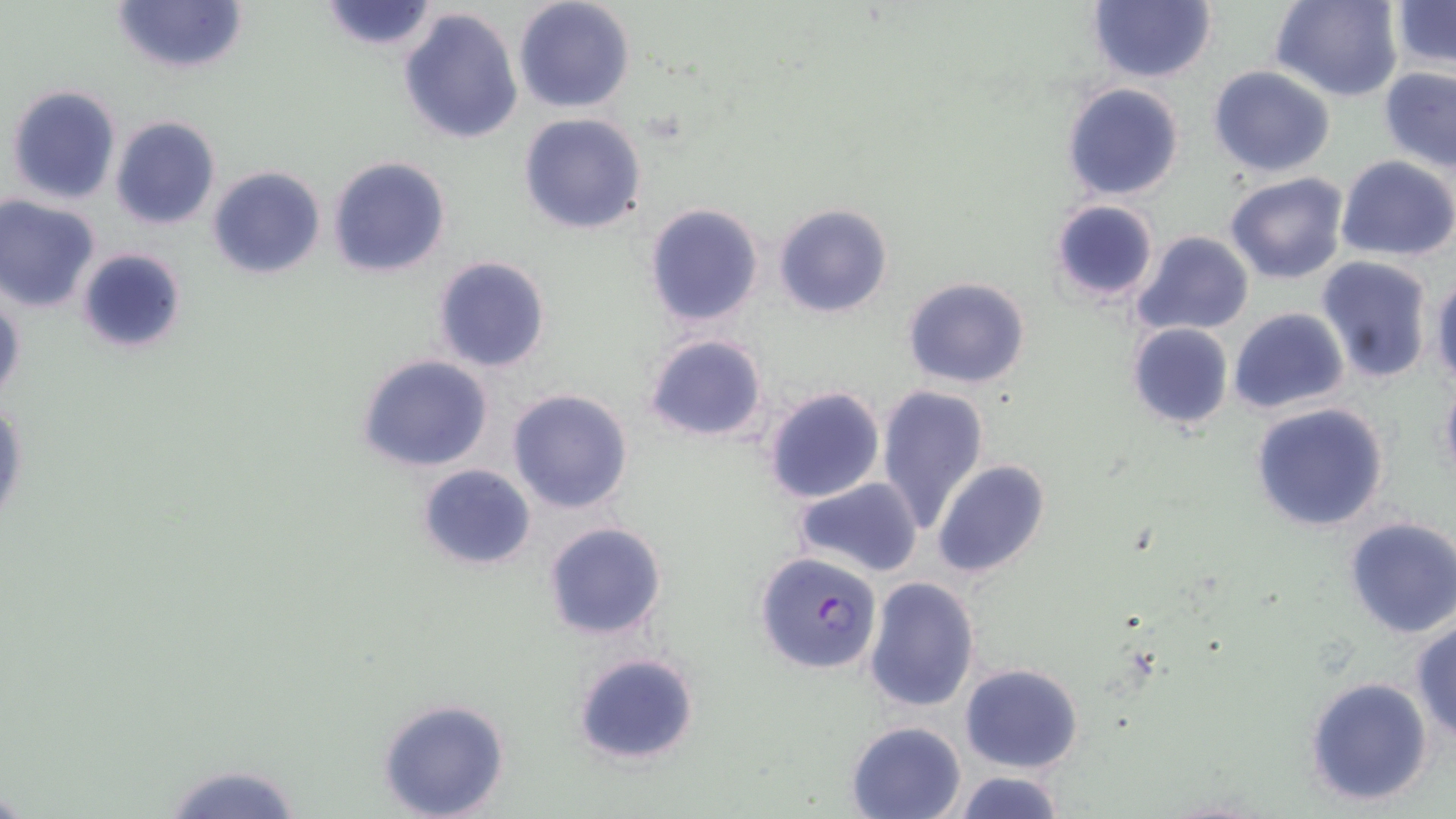

Approximate bounding boxes as (x1,y1)-(x2,y2) corner pairs in pixels. Uninfected red blood cell locations: (315,0)-(444,53), (512,0)-(635,114), (1086,0)-(1215,84), (1269,0)-(1403,102), (111,1)-(248,74), (1391,1)-(1455,72), (397,6)-(524,145), (1208,66)-(1335,177), (1379,68)-(1456,173), (1061,82)-(1186,202), (4,83)-(123,206), (518,112)-(647,235), (109,116)-(221,232), (1334,155)-(1456,261), (326,156)-(452,279), (206,166)-(327,280), (1223,172)-(1349,285), (0,194)-(102,314), (1049,197)-(1160,305), (644,203)-(764,328), (773,203)-(892,318), (1132,232)-(1254,338), (75,247)-(187,355), (431,254)-(552,374), (1316,255)-(1436,385), (1429,269)-(1456,390), (902,276)-(1031,388), (0,287)-(26,412), (1228,307)-(1349,416), (1126,323)-(1234,432), (642,334)-(768,442), (356,354)-(495,474), (1438,371)-(1456,486), (876,384)-(989,531), (761,386)-(886,503), (506,388)-(634,515), (1248,403)-(1391,534), (932,460)-(1051,580), (416,464)-(536,571), (792,477)-(923,578), (1342,517)-(1456,639), (543,521)-(668,641), (862,575)-(980,711), (1409,617)-(1456,741), (573,651)-(698,765), (960,663)-(1084,773), (1305,675)-(1434,807), (375,697)-(512,819), (844,720)-(967,819), (156,761)-(307,819), (950,772)-(1067,818). Plasmodium falciparum-infected red blood cell locations: (754,551)-(883,675). Slide-level diagnosis: Plasmodium falciparum. Light microscopy. Thin blood smear. Single field of view. Captured at 1000x magnification. Image is 1456×819 pixels. May-Grünwald-Giemsa-stained preparation.